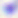 Toxoplasma gondii is seen. 400x magnification. Photomicrograph.